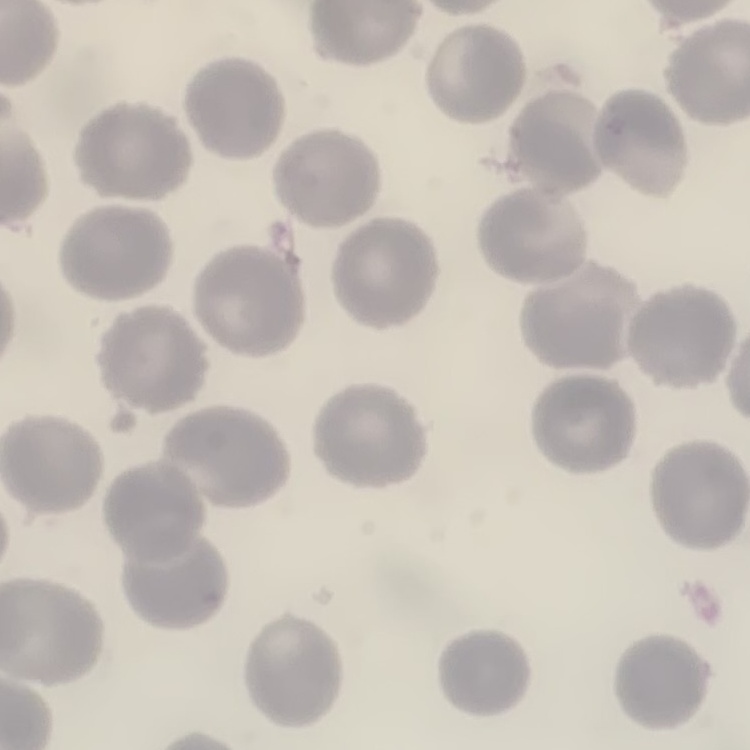 The erythrocytes show no rouleaux formation. Field's or Giemsa stain. Square crop of a larger photomicrograph. Thin blood film.